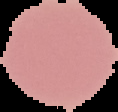

Summary:
  - Preparation: thin blood film
  - Image type: segmented cell region with the area outside set to black
  - Image size: 118×112 pixels
  - Result: negative for malaria parasites